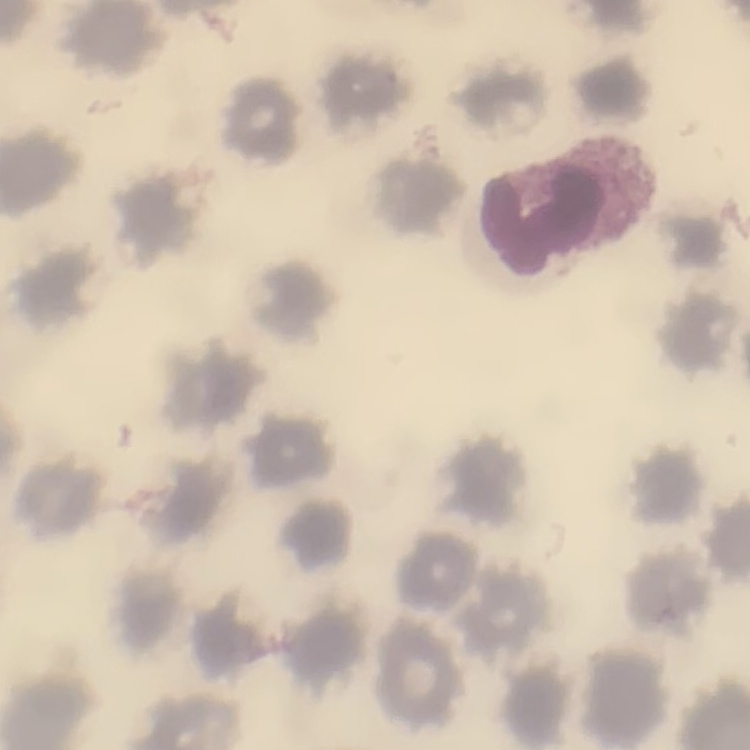
The red blood cells exhibit no rouleaux formation. Field's or Giemsa stain. Thin blood film. One tile cut from a larger photomicrograph.